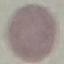

Summary:
  - Result: negative for malaria parasites
  - Capture: smartphone through the microscope eyepiece
  - Stain: Giemsa
  - Image type: cell patch, automatically extracted from a larger field of view and resized to 64 × 64 pixels
  - Preparation: thin blood film